Locate every Plasmodium parasite.
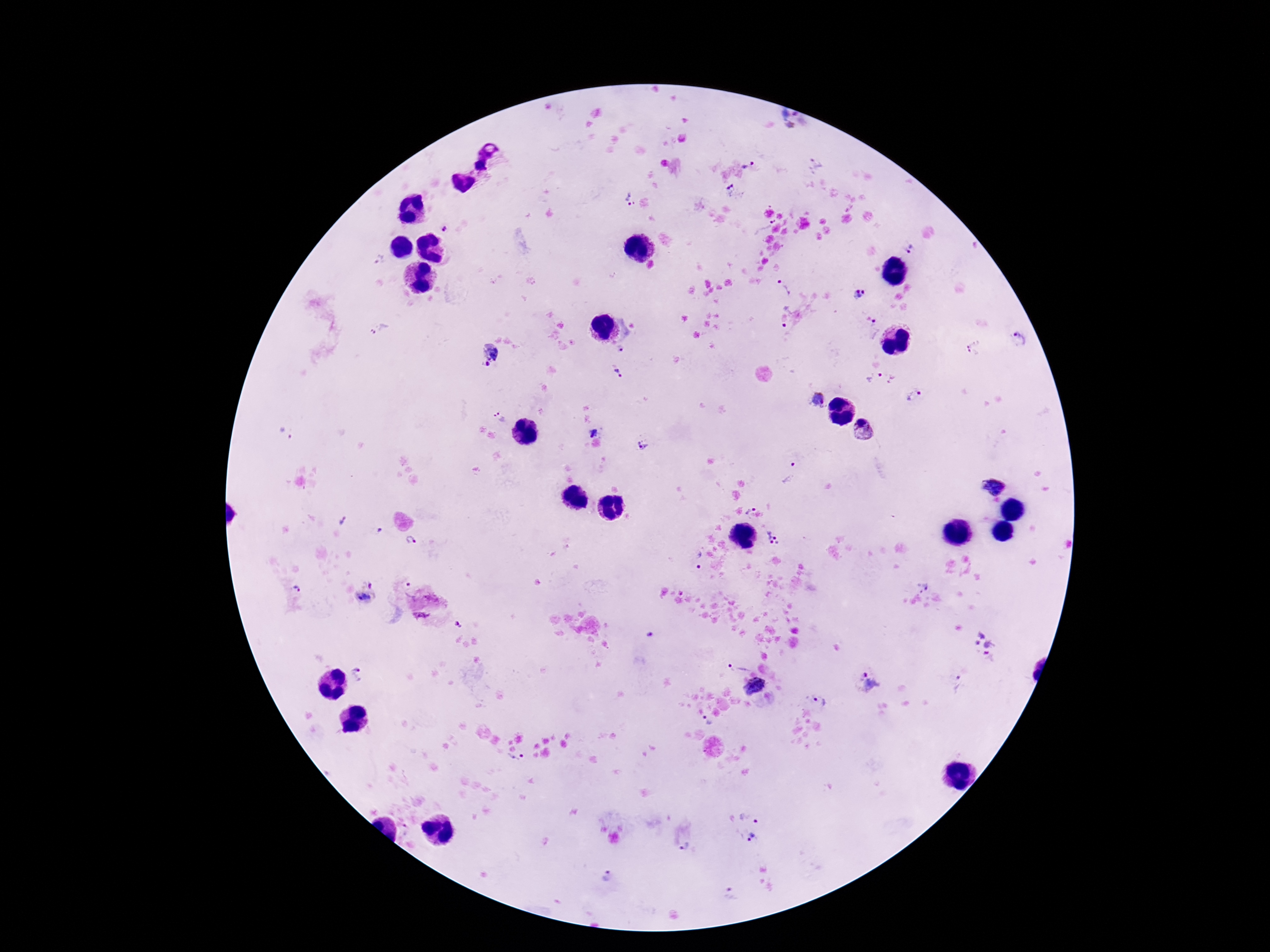
Approximate centers as {x, y} in pixels.
Plasmodium parasites: {797, 122}, {817, 164}, {748, 165}, {732, 192}, {629, 200}, {764, 226}, {444, 228}, {910, 250}, {380, 260}, {784, 287}, {857, 293}, {782, 314}, {872, 329}, {381, 330}, {1021, 338}, {971, 340}, {622, 349}, {488, 354}, {972, 355}, {621, 373}, {874, 376}, {915, 396}, {816, 398}, {501, 418}, {864, 430}, {593, 431}, {287, 433}, {643, 444}, {790, 473}, {995, 487}, {750, 508}, {346, 524}, {774, 540}, {412, 541}, {697, 560}, {922, 584}, {298, 589}, {369, 593}, {421, 616}, {459, 625}, {649, 635}, {984, 642}, {741, 666}, {356, 674}, {867, 682}, {957, 685}, {753, 686}, {820, 701}, {707, 721}, {517, 760}, {751, 814}, {752, 838}, {687, 847}, {606, 874}, {732, 892}.

Giemsa stain. Thick blood film. Image is 1270×952 pixels. Patient malaria status: positive. Smartphone photograph taken through the microscope eyepiece. 100x magnification. One field from this slide.